Locate every Plasmodium falciparum-infected red blood cell.
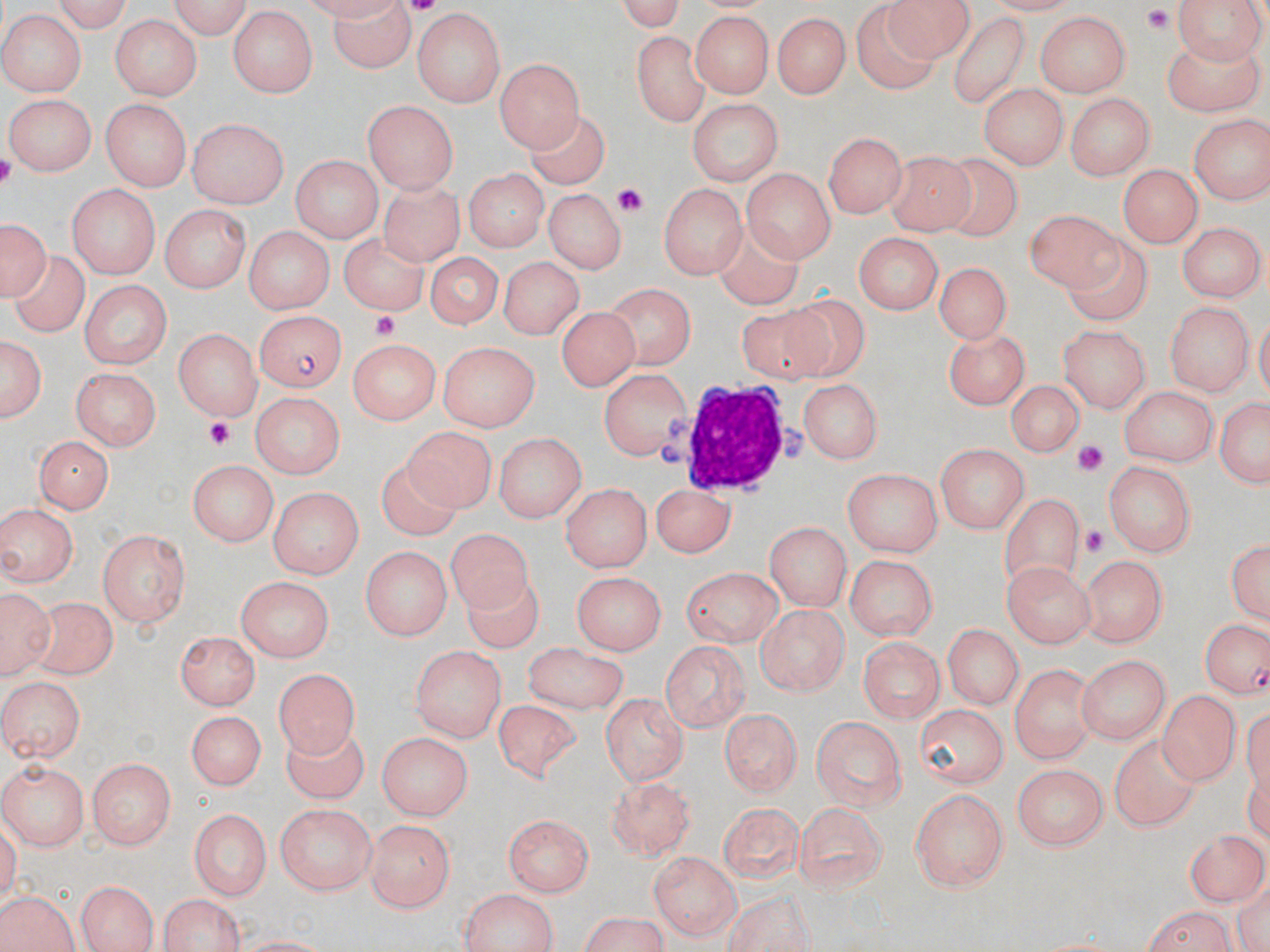

Approximate bounding boxes as [x1, y1, x2, y2] in pixels.
Plasmodium falciparum-infected red blood cells: [256, 312, 346, 391], [1204, 620, 1270, 697].

slide-level diagnosis = Plasmodium falciparum
image size = 1270×952 pixels
stain = May-Grünwald-Giemsa
magnification = 1000x
modality = optical microscopy
preparation = thin blood smear
field of view = single
uninfected red blood cell locations = approximate bounding boxes as [x1, y1, x2, y2] in pixels: [38, 0, 137, 30], [167, 0, 256, 39], [611, 0, 693, 33], [886, 0, 975, 59], [1169, 0, 1264, 67], [325, 1, 418, 73], [413, 9, 503, 104], [228, 10, 315, 96], [689, 10, 776, 99], [949, 10, 1032, 109], [773, 11, 850, 97], [856, 11, 939, 93], [1033, 11, 1129, 97], [0, 12, 85, 97], [109, 14, 200, 101], [1158, 29, 1268, 114], [628, 30, 712, 125], [497, 56, 584, 152], [980, 84, 1065, 171], [1066, 93, 1154, 180], [2, 94, 93, 174], [685, 98, 785, 183], [102, 100, 193, 187], [362, 101, 459, 193], [9, 106, 179, 178], [528, 113, 608, 190], [1187, 113, 1270, 204], [189, 119, 290, 208], [822, 133, 903, 219], [884, 152, 979, 239], [287, 154, 380, 241], [941, 155, 1023, 235], [1120, 163, 1201, 249], [741, 165, 835, 261], [463, 170, 547, 253], [373, 178, 461, 265], [660, 180, 744, 282], [67, 184, 160, 278], [546, 191, 623, 272], [161, 207, 248, 293], [1023, 209, 1131, 296], [1, 217, 49, 301], [711, 220, 803, 312], [1179, 224, 1261, 300], [241, 225, 336, 312], [347, 232, 434, 311], [851, 232, 941, 316], [1068, 232, 1156, 321], [421, 250, 503, 328], [12, 256, 89, 334], [497, 256, 580, 339], [932, 262, 1015, 341], [79, 281, 171, 368], [608, 281, 695, 371], [97, 291, 243, 387], [768, 298, 871, 377], [735, 303, 839, 376], [1164, 304, 1254, 395], [554, 305, 643, 390], [1056, 323, 1151, 412], [172, 327, 260, 421], [941, 329, 1029, 409], [1, 330, 48, 428], [349, 337, 441, 423], [437, 341, 537, 431], [72, 366, 161, 449], [599, 367, 695, 461], [1005, 382, 1085, 456], [802, 383, 879, 462], [1119, 384, 1217, 468], [249, 390, 344, 480], [1213, 392, 1269, 492], [400, 425, 496, 511], [495, 431, 585, 523], [35, 434, 113, 514], [936, 444, 1030, 533], [187, 460, 277, 548], [378, 460, 463, 542], [1105, 463, 1196, 557], [842, 468, 942, 556], [649, 480, 731, 557], [560, 483, 651, 571], [268, 486, 365, 580], [1002, 494, 1082, 602], [3, 504, 77, 592], [765, 522, 850, 610], [452, 527, 536, 609], [98, 528, 190, 627], [1226, 534, 1270, 628], [359, 545, 450, 640], [1079, 553, 1167, 648], [844, 556, 936, 641], [1005, 561, 1093, 647], [681, 566, 782, 647], [462, 573, 545, 651], [574, 573, 664, 654], [238, 577, 334, 661], [0, 585, 53, 682], [32, 598, 121, 676], [753, 605, 851, 691], [944, 623, 1024, 712], [174, 632, 256, 710], [861, 637, 942, 726], [659, 639, 750, 729], [520, 640, 630, 714], [412, 647, 504, 743], [1080, 655, 1171, 745], [1007, 663, 1095, 762], [273, 664, 361, 751], [0, 676, 83, 762], [1156, 689, 1239, 786], [600, 691, 687, 787], [492, 700, 578, 782], [914, 704, 1008, 785], [718, 705, 802, 799], [182, 710, 267, 793], [812, 716, 909, 811], [280, 726, 369, 798], [372, 731, 469, 817], [1110, 731, 1201, 833], [85, 757, 176, 851], [1, 759, 88, 852], [1012, 765, 1109, 853], [608, 775, 697, 860], [910, 789, 1010, 893], [716, 803, 803, 884], [795, 803, 887, 895], [273, 804, 373, 896], [189, 808, 271, 902], [504, 812, 593, 897], [364, 819, 453, 911], [1183, 825, 1265, 905], [649, 851, 741, 940], [75, 879, 157, 952], [456, 887, 562, 951], [719, 887, 821, 949], [0, 888, 83, 952], [156, 894, 250, 951], [1134, 906, 1239, 952], [570, 915, 673, 952]
platelet locations = approximate bounding boxes as [x1, y1, x2, y2] in pixels: [1143, 6, 1174, 34], [615, 186, 644, 213], [367, 309, 397, 337], [203, 416, 234, 447], [1075, 442, 1106, 472], [1078, 526, 1106, 554]
white blood cell locations = approximate bounding boxes as [x1, y1, x2, y2] in pixels: [662, 379, 811, 496]